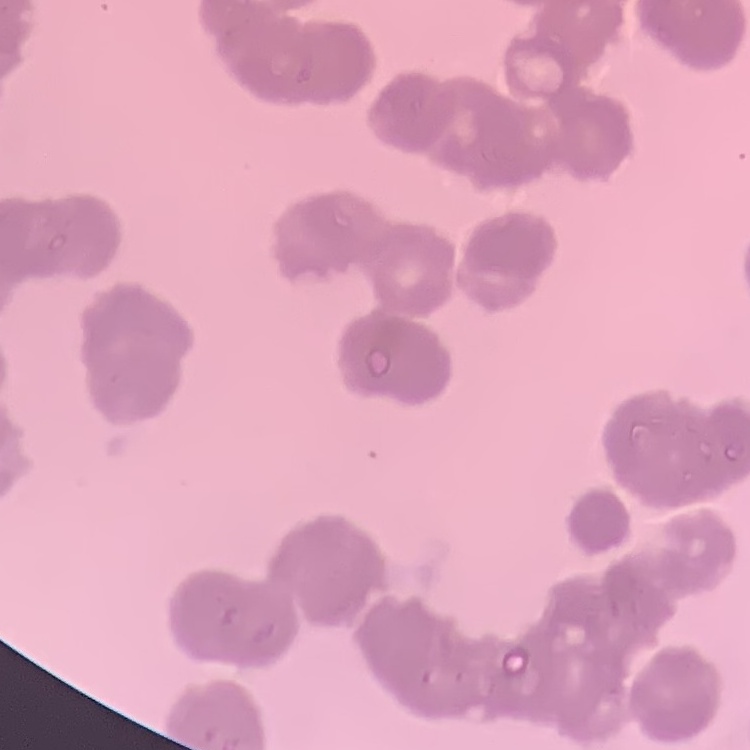

Summary:
  - Red blood cell morphology: rouleaux formation
  - Preparation: thin peripheral smear
  - Stain: Field's or Giemsa
  - Image type: one tile cut from a larger photomicrograph